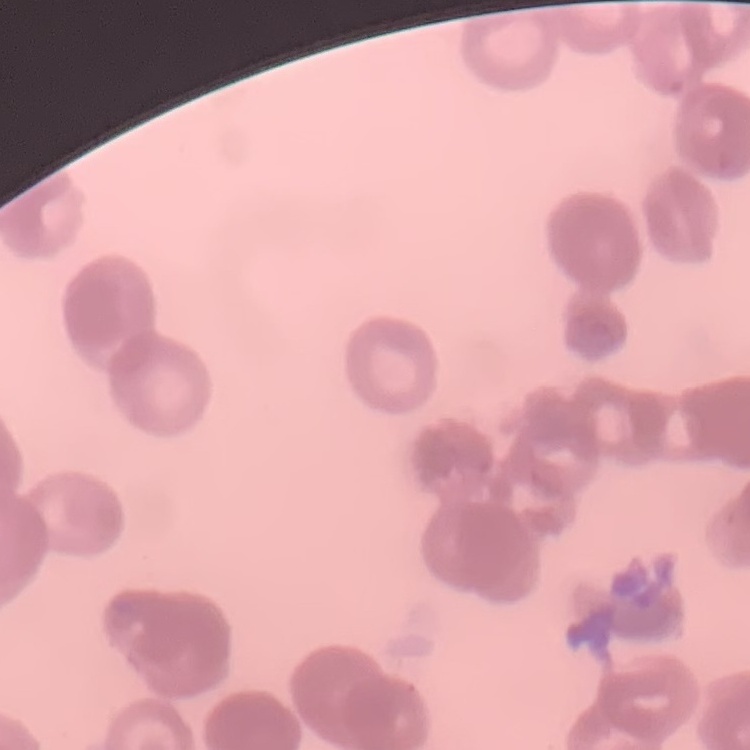

red blood cell morphology = rouleaux formation
image type = square crop of a larger photomicrograph
stain = Field's or Giemsa
preparation = thin peripheral smear